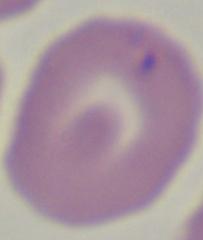
identification = Babesia
modality = photomicrograph
magnification = 1000x